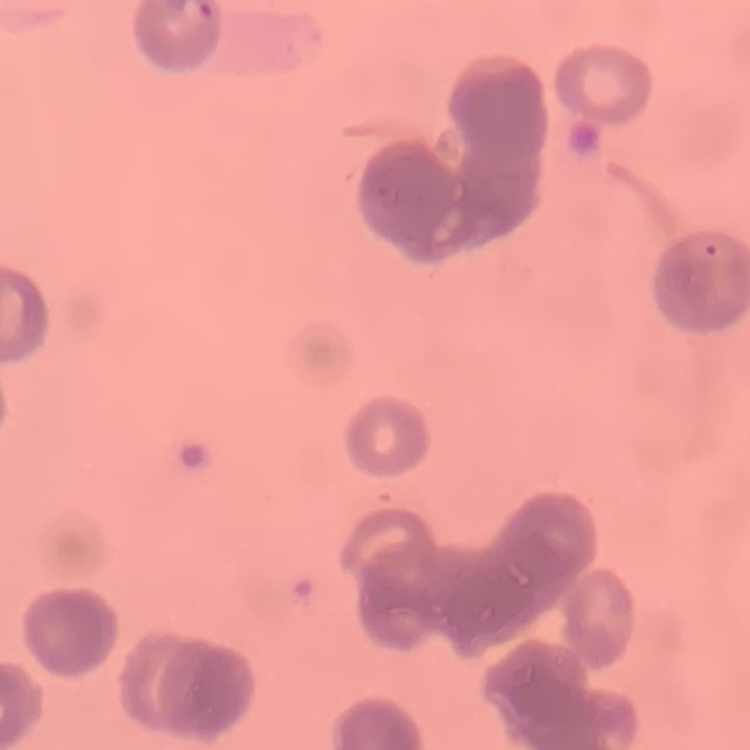

red blood cell morphology = rouleaux formation
stain = Field's or Giemsa
image type = one tile cut from a larger photomicrograph
preparation = thin blood film